Name the blood parasite species.
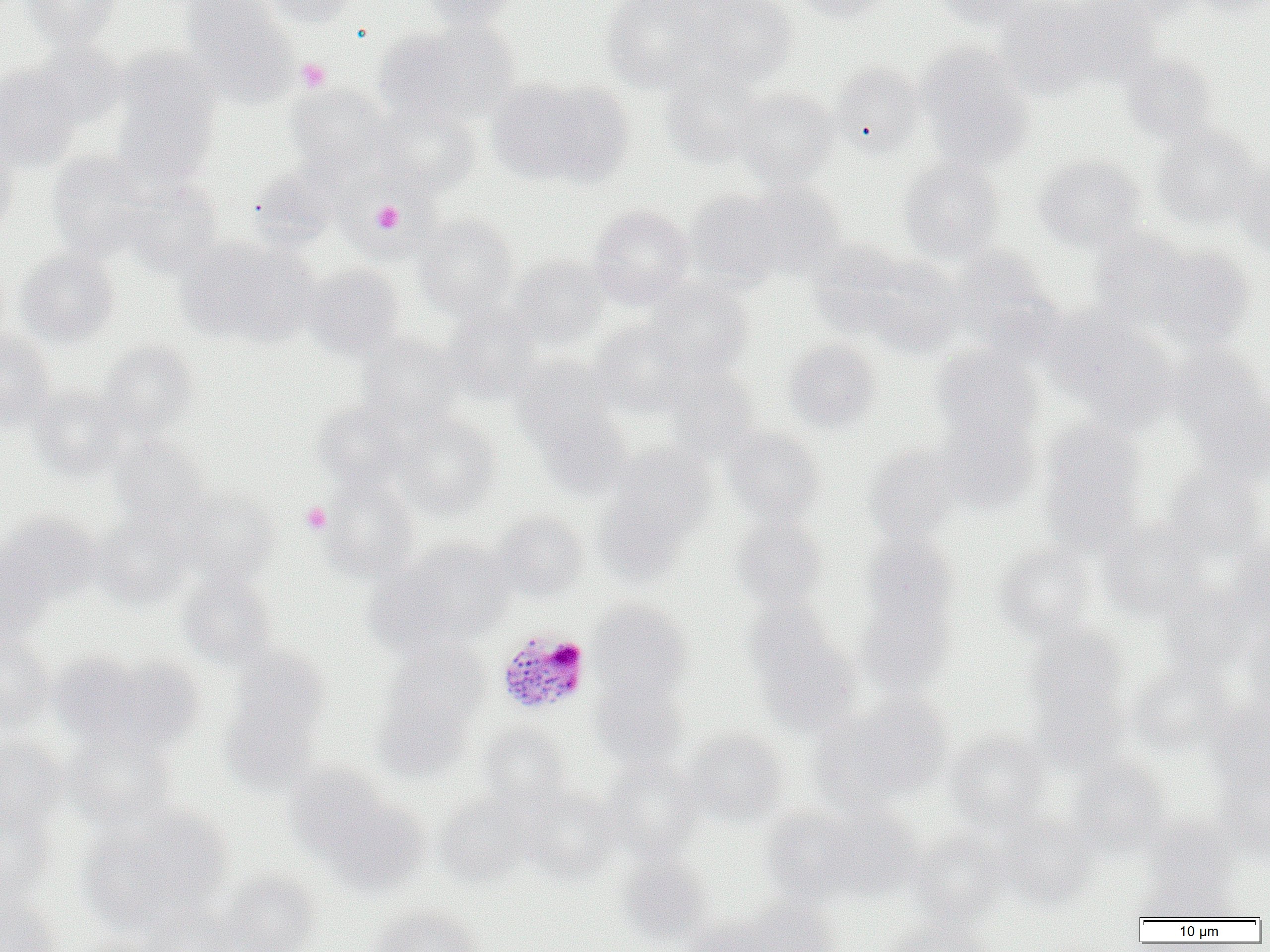

Plasmodium malariae.

image size = 1270×952 pixels
Plasmodium malariae-infected red blood cell locations = approximate bounding boxes as named x1/y1/x2/y2 corners in pixels: (x1=496, y1=629, x2=592, y2=716)
modality = light microscopy
uninfected red blood cell locations = approximate bounding boxes as named x1/y1/x2/y2 corners in pixels: (x1=20, y1=0, x2=122, y2=48), (x1=180, y1=0, x2=296, y2=100), (x1=259, y1=0, x2=361, y2=27), (x1=421, y1=0, x2=520, y2=30), (x1=685, y1=0, x2=798, y2=85), (x1=790, y1=0, x2=894, y2=21), (x1=932, y1=0, x2=1041, y2=32), (x1=1061, y1=0, x2=1163, y2=81), (x1=1192, y1=0, x2=1270, y2=18), (x1=600, y1=1, x2=720, y2=93), (x1=995, y1=1, x2=1100, y2=95), (x1=376, y1=22, x2=519, y2=129), (x1=29, y1=42, x2=128, y2=131), (x1=915, y1=43, x2=1035, y2=171), (x1=1120, y1=54, x2=1219, y2=144), (x1=111, y1=56, x2=221, y2=186), (x1=829, y1=61, x2=924, y2=159), (x1=0, y1=64, x2=83, y2=170), (x1=660, y1=67, x2=766, y2=167), (x1=487, y1=77, x2=629, y2=188), (x1=286, y1=84, x2=394, y2=178), (x1=732, y1=88, x2=839, y2=187), (x1=372, y1=105, x2=481, y2=197), (x1=1152, y1=125, x2=1263, y2=229), (x1=0, y1=135, x2=18, y2=240), (x1=46, y1=150, x2=156, y2=259), (x1=1033, y1=155, x2=1146, y2=251), (x1=1234, y1=156, x2=1270, y2=258), (x1=897, y1=159, x2=1004, y2=263), (x1=247, y1=166, x2=341, y2=253), (x1=123, y1=176, x2=224, y2=277), (x1=737, y1=181, x2=845, y2=278), (x1=684, y1=188, x2=795, y2=288), (x1=588, y1=205, x2=695, y2=307), (x1=414, y1=215, x2=518, y2=318), (x1=1089, y1=229, x2=1198, y2=329), (x1=176, y1=235, x2=315, y2=347), (x1=807, y1=239, x2=910, y2=337), (x1=1148, y1=247, x2=1255, y2=347), (x1=14, y1=249, x2=120, y2=347), (x1=951, y1=249, x2=1061, y2=358), (x1=857, y1=253, x2=965, y2=357), (x1=507, y1=255, x2=610, y2=350), (x1=303, y1=262, x2=406, y2=359), (x1=645, y1=281, x2=753, y2=378), (x1=442, y1=305, x2=543, y2=403), (x1=1048, y1=313, x2=1180, y2=427), (x1=590, y1=321, x2=696, y2=417), (x1=0, y1=331, x2=57, y2=431), (x1=358, y1=333, x2=462, y2=424), (x1=784, y1=338, x2=882, y2=433), (x1=96, y1=340, x2=198, y2=437), (x1=931, y1=345, x2=1044, y2=445), (x1=1174, y1=350, x2=1268, y2=475), (x1=510, y1=355, x2=618, y2=451), (x1=665, y1=365, x2=760, y2=459), (x1=30, y1=387, x2=127, y2=481), (x1=314, y1=402, x2=409, y2=492), (x1=534, y1=404, x2=632, y2=500), (x1=392, y1=411, x2=500, y2=519), (x1=933, y1=416, x2=1039, y2=513), (x1=1037, y1=422, x2=1147, y2=550), (x1=721, y1=425, x2=827, y2=524), (x1=111, y1=438, x2=211, y2=529), (x1=607, y1=444, x2=714, y2=538), (x1=865, y1=446, x2=961, y2=546), (x1=1159, y1=464, x2=1266, y2=561), (x1=319, y1=475, x2=420, y2=581), (x1=176, y1=489, x2=280, y2=585), (x1=593, y1=494, x2=692, y2=588), (x1=2, y1=512, x2=104, y2=605), (x1=491, y1=512, x2=589, y2=602), (x1=91, y1=513, x2=191, y2=608), (x1=730, y1=513, x2=828, y2=612), (x1=1098, y1=522, x2=1207, y2=622), (x1=1226, y1=533, x2=1269, y2=632), (x1=860, y1=535, x2=959, y2=634), (x1=375, y1=540, x2=514, y2=653), (x1=0, y1=542, x2=52, y2=646), (x1=993, y1=543, x2=1096, y2=642), (x1=177, y1=572, x2=280, y2=670), (x1=855, y1=572, x2=959, y2=693), (x1=1158, y1=580, x2=1258, y2=675), (x1=588, y1=601, x2=692, y2=697), (x1=747, y1=612, x2=860, y2=732), (x1=1240, y1=617, x2=1270, y2=715), (x1=1025, y1=625, x2=1128, y2=720), (x1=0, y1=634, x2=55, y2=735), (x1=377, y1=640, x2=490, y2=756), (x1=57, y1=652, x2=203, y2=757), (x1=220, y1=653, x2=330, y2=787), (x1=1127, y1=662, x2=1232, y2=755), (x1=588, y1=672, x2=690, y2=770), (x1=1028, y1=679, x2=1129, y2=773), (x1=825, y1=693, x2=952, y2=802), (x1=1205, y1=698, x2=1270, y2=792), (x1=477, y1=723, x2=572, y2=812), (x1=684, y1=727, x2=790, y2=827), (x1=64, y1=731, x2=179, y2=830), (x1=944, y1=731, x2=1051, y2=832), (x1=0, y1=735, x2=69, y2=835), (x1=1067, y1=757, x2=1172, y2=857), (x1=599, y1=758, x2=704, y2=859), (x1=282, y1=761, x2=389, y2=858), (x1=1215, y1=770, x2=1270, y2=861), (x1=520, y1=786, x2=622, y2=882), (x1=437, y1=792, x2=536, y2=887), (x1=323, y1=798, x2=431, y2=894), (x1=817, y1=802, x2=922, y2=897), (x1=0, y1=803, x2=55, y2=907), (x1=759, y1=804, x2=867, y2=905), (x1=80, y1=805, x2=232, y2=933), (x1=996, y1=815, x2=1099, y2=909), (x1=1143, y1=815, x2=1240, y2=902), (x1=908, y1=830, x2=1010, y2=925), (x1=616, y1=856, x2=715, y2=947), (x1=221, y1=870, x2=321, y2=952), (x1=1135, y1=873, x2=1238, y2=921), (x1=0, y1=893, x2=63, y2=952), (x1=138, y1=899, x2=240, y2=952), (x1=742, y1=900, x2=842, y2=952), (x1=367, y1=905, x2=486, y2=952), (x1=680, y1=916, x2=776, y2=952), (x1=880, y1=917, x2=990, y2=952), (x1=64, y1=938, x2=170, y2=952)
field of view = one of a larger specimen
platelet locations = approximate bounding boxes as named x1/y1/x2/y2 corners in pixels: (x1=296, y1=58, x2=331, y2=92), (x1=360, y1=189, x2=420, y2=245), (x1=368, y1=200, x2=408, y2=234), (x1=300, y1=502, x2=332, y2=535)
preparation = thin blood smear
magnification = 1000x